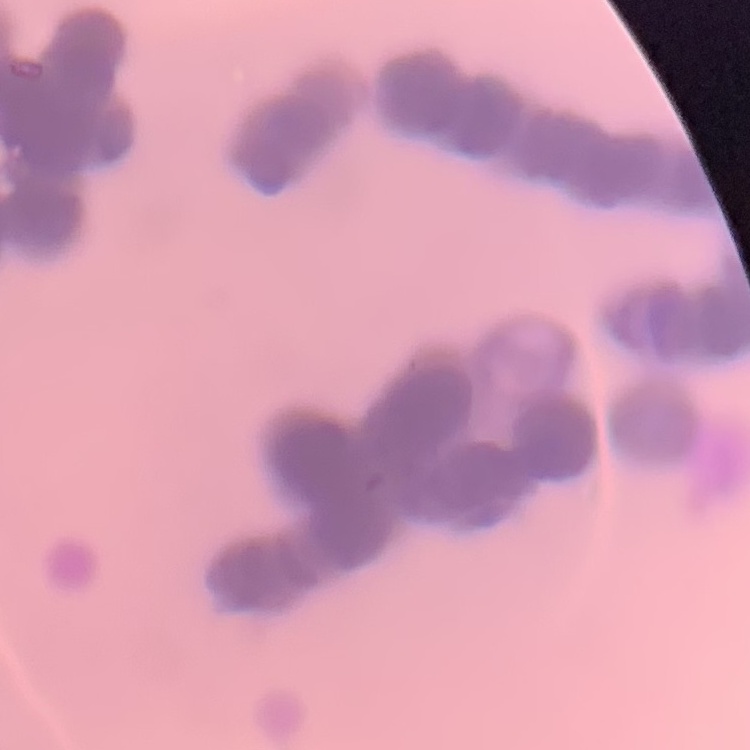 The erythrocytes exhibit rouleaux formation. Stained with either Field's or Giemsa. Square crop of a larger photomicrograph. Thin peripheral smear.